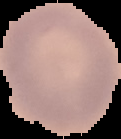

Summary:
  - Preparation: thin blood film
  - Image size: 121×139 pixels
  - Image type: cell region segmented out of the field of view; surrounding area masked to black
  - Result: no Plasmodium parasites detected